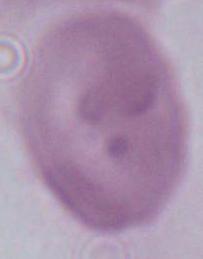

An erythrocyte is shown. Photomicrograph. Captured at 1000x magnification.